Locate every blood parasite and identify its species.
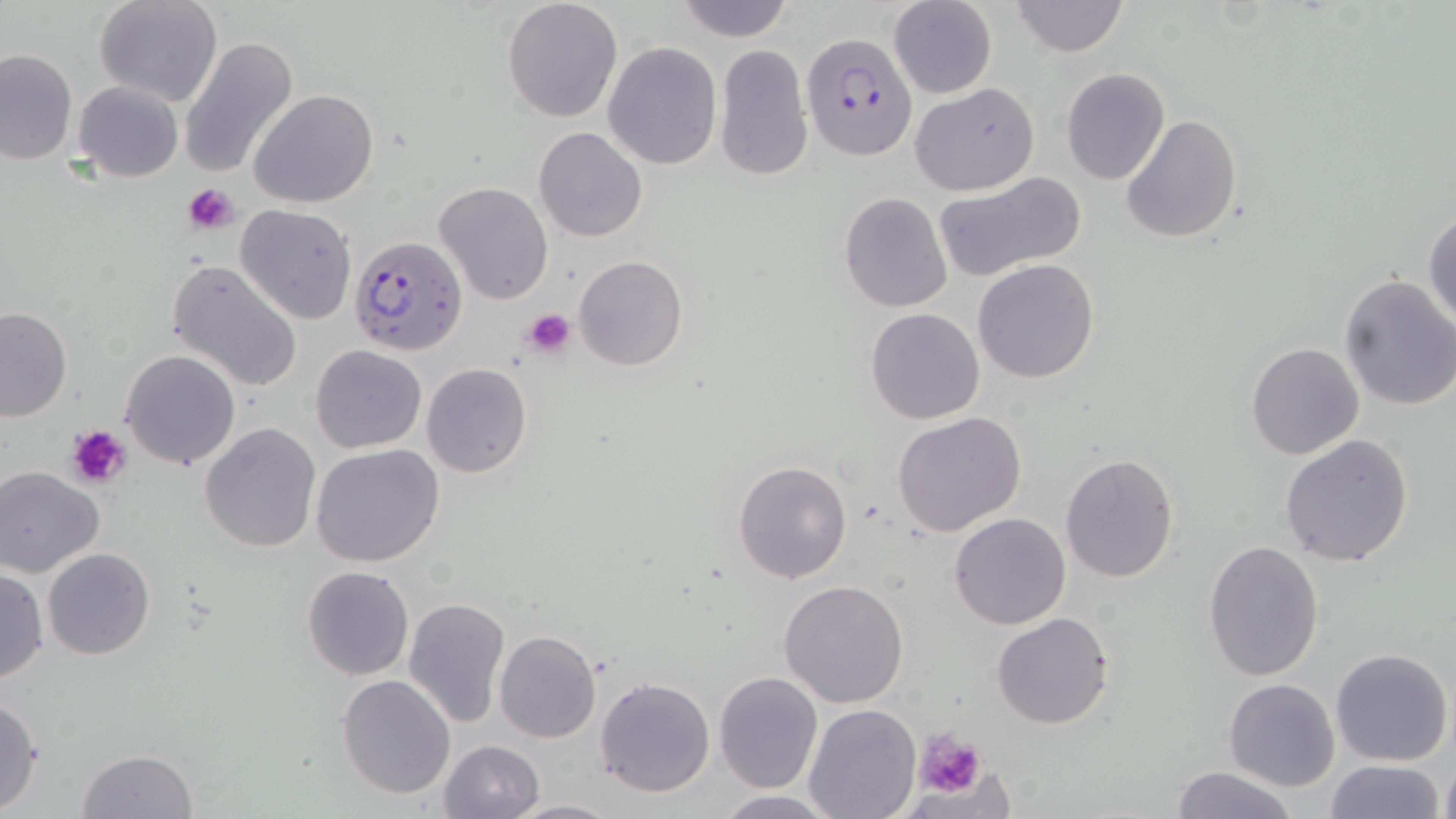

Approximate bounding boxes as named x1/y1/x2/y2 corners in pixels.
Plasmodium falciparum-infected red blood cells: (x1=802, y1=32, x2=917, y2=162), (x1=349, y1=234, x2=467, y2=356).
No Plasmodium ovale, Plasmodium malariae, Plasmodium vivax, Babesia divergens, or Trypanosoma brucei observed.

slide_level_diagnosis: Plasmodium falciparum
preparation: thin blood film
image_size: 1456×819 pixels
field_of_view: single
uninfected_red_blood_cell_locations: 'approximate bounding boxes as named x1/y1/x2/y2 corners in pixels: (x1=95, y1=0, x2=221, y2=106), (x1=503, y1=0, x2=623, y2=123), (x1=888, y1=0, x2=997, y2=99), (x1=1011, y1=0, x2=1128, y2=58), (x1=672, y1=1, x2=797, y2=43), (x1=179, y1=34, x2=299, y2=182), (x1=603, y1=42, x2=722, y2=169), (x1=714, y1=43, x2=812, y2=182), (x1=0, y1=47, x2=77, y2=164), (x1=1060, y1=67, x2=1170, y2=185), (x1=73, y1=80, x2=184, y2=183), (x1=910, y1=83, x2=1040, y2=197), (x1=249, y1=90, x2=378, y2=208), (x1=1121, y1=113, x2=1242, y2=243), (x1=534, y1=126, x2=648, y2=242), (x1=933, y1=171, x2=1088, y2=285), (x1=434, y1=181, x2=553, y2=304), (x1=839, y1=191, x2=953, y2=312), (x1=235, y1=203, x2=357, y2=324), (x1=1424, y1=208, x2=1456, y2=328), (x1=572, y1=255, x2=689, y2=371), (x1=167, y1=258, x2=303, y2=393), (x1=972, y1=259, x2=1100, y2=385), (x1=1336, y1=275, x2=1456, y2=411), (x1=0, y1=306, x2=72, y2=422), (x1=865, y1=308, x2=984, y2=424), (x1=1245, y1=341, x2=1364, y2=460), (x1=311, y1=344, x2=426, y2=454), (x1=120, y1=348, x2=241, y2=471), (x1=422, y1=363, x2=531, y2=478), (x1=892, y1=411, x2=1027, y2=536), (x1=200, y1=422, x2=320, y2=552), (x1=1279, y1=434, x2=1415, y2=568), (x1=312, y1=444, x2=444, y2=567), (x1=1060, y1=451, x2=1180, y2=582), (x1=733, y1=460, x2=853, y2=584), (x1=0, y1=466, x2=104, y2=577), (x1=950, y1=511, x2=1071, y2=629), (x1=1203, y1=539, x2=1326, y2=681), (x1=44, y1=547, x2=155, y2=659), (x1=1, y1=565, x2=49, y2=685), (x1=302, y1=565, x2=414, y2=681), (x1=778, y1=579, x2=909, y2=707), (x1=402, y1=597, x2=510, y2=728), (x1=991, y1=611, x2=1114, y2=730), (x1=495, y1=630, x2=601, y2=743), (x1=1330, y1=647, x2=1453, y2=766), (x1=714, y1=670, x2=824, y2=793), (x1=336, y1=673, x2=455, y2=799), (x1=594, y1=675, x2=718, y2=798), (x1=1223, y1=677, x2=1341, y2=790), (x1=0, y1=695, x2=45, y2=815), (x1=805, y1=702, x2=922, y2=819), (x1=439, y1=739, x2=546, y2=819), (x1=77, y1=748, x2=197, y2=818), (x1=1438, y1=756, x2=1456, y2=819), (x1=1323, y1=759, x2=1447, y2=818), (x1=1167, y1=765, x2=1300, y2=819), (x1=711, y1=791, x2=837, y2=818), (x1=507, y1=796, x2=620, y2=817)'
stain: May-Grünwald-Giemsa
platelet_locations: 'approximate bounding boxes as named x1/y1/x2/y2 corners in pixels: (x1=182, y1=182, x2=238, y2=233), (x1=523, y1=308, x2=575, y2=358), (x1=67, y1=425, x2=133, y2=490), (x1=915, y1=729, x2=985, y2=798)'
magnification: 1000x
modality: light microscopy